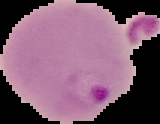
Segmented cell region on a black background. From a thin blood smear. Result: malaria parasites detected. Image is 160×124 pixels.